Outline each blood parasite and name the species.
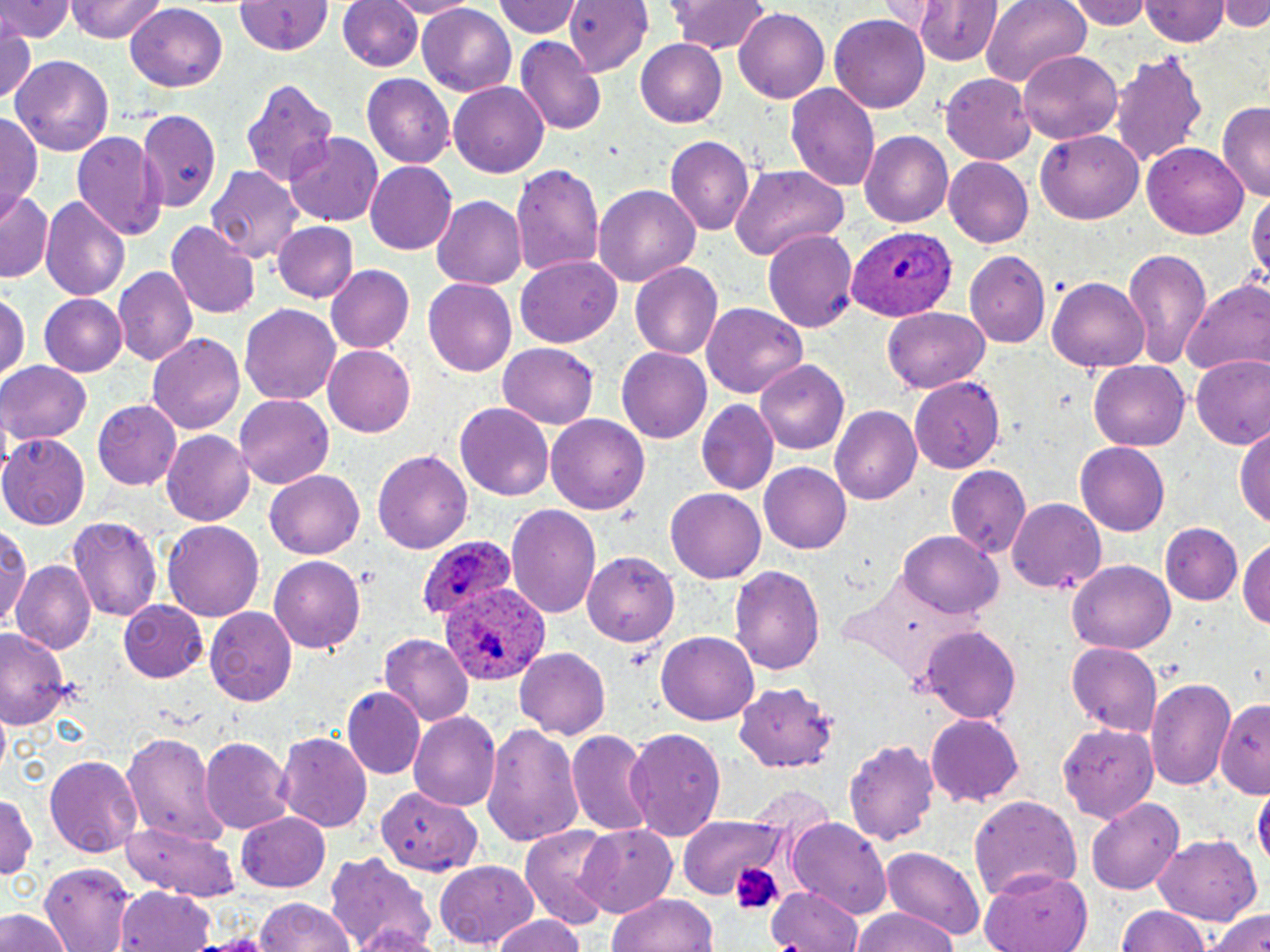
Approximate bounding boxes as [x1, y1, x2, y2] in pixels.
Plasmodium ovale-infected red blood cells: [848, 227, 956, 321], [420, 536, 516, 619], [444, 582, 551, 684].
No Plasmodium falciparum, Plasmodium malariae, Plasmodium vivax, Babesia divergens, or Trypanosoma brucei observed.

Uninfected red blood cell locations: [0, 0, 73, 42], [67, 0, 167, 42], [233, 0, 335, 55], [389, 0, 478, 17], [492, 0, 584, 39], [564, 0, 654, 75], [668, 0, 772, 54], [877, 0, 944, 37], [1071, 0, 1154, 31], [1219, 0, 1270, 29], [338, 1, 420, 73], [982, 1, 1090, 88], [1141, 1, 1230, 47], [911, 2, 1006, 66], [418, 5, 517, 95], [125, 6, 229, 91], [735, 7, 829, 103], [830, 14, 931, 112], [0, 20, 38, 104], [517, 34, 608, 137], [635, 38, 728, 129], [1112, 50, 1209, 168], [1018, 51, 1123, 145], [12, 55, 115, 156], [942, 72, 1037, 163], [361, 75, 455, 166], [240, 78, 338, 187], [449, 83, 549, 177], [787, 83, 880, 196], [1217, 102, 1270, 203], [138, 110, 221, 212], [0, 114, 42, 213], [72, 129, 166, 241], [1036, 129, 1144, 223], [286, 131, 387, 225], [861, 132, 952, 228], [665, 136, 753, 237], [1142, 145, 1250, 238], [945, 157, 1033, 248], [511, 162, 606, 276], [205, 163, 307, 265], [365, 163, 457, 253], [729, 164, 848, 262], [592, 185, 700, 288], [1246, 185, 1269, 290], [2, 191, 56, 284], [41, 196, 130, 303], [432, 196, 528, 289], [167, 221, 260, 317], [271, 223, 357, 302], [763, 228, 859, 332], [1121, 249, 1211, 366], [966, 251, 1051, 345], [516, 259, 621, 346], [629, 263, 721, 359], [326, 265, 414, 353], [112, 267, 195, 366], [1048, 277, 1148, 372], [422, 279, 516, 377], [1183, 282, 1269, 378], [0, 290, 27, 383], [39, 295, 127, 377], [239, 302, 341, 405], [702, 302, 807, 398], [885, 307, 993, 393], [147, 331, 245, 433], [498, 342, 599, 428], [323, 344, 416, 437], [617, 349, 712, 442], [1190, 358, 1269, 451], [756, 360, 850, 452], [1088, 360, 1191, 451], [0, 362, 91, 444], [907, 377, 1007, 471], [233, 393, 335, 491], [92, 398, 182, 490], [697, 399, 777, 495], [455, 402, 555, 502], [832, 405, 922, 507], [545, 415, 649, 516], [1235, 426, 1270, 528], [162, 431, 255, 525], [0, 434, 88, 527], [1075, 442, 1168, 537], [373, 445, 473, 554], [759, 462, 852, 555], [947, 466, 1032, 559], [265, 469, 366, 559], [666, 489, 766, 583], [1007, 497, 1107, 592], [507, 504, 601, 620], [67, 516, 161, 620], [1, 520, 31, 632], [164, 520, 263, 618], [1161, 522, 1241, 604], [899, 529, 1001, 618], [1242, 534, 1270, 630], [584, 552, 679, 646], [267, 553, 370, 656], [1069, 559, 1177, 654], [12, 561, 96, 656], [730, 564, 825, 676], [119, 599, 209, 682], [205, 605, 296, 704], [920, 627, 1022, 722], [0, 628, 74, 729], [655, 632, 757, 728], [377, 633, 472, 725], [1065, 640, 1164, 738], [515, 648, 611, 738], [1147, 676, 1233, 789], [735, 681, 839, 774], [344, 688, 426, 779], [1217, 702, 1269, 798], [409, 711, 499, 811], [926, 711, 1025, 804], [480, 721, 585, 848], [1056, 722, 1161, 823], [566, 729, 657, 837], [624, 729, 727, 840], [274, 730, 373, 833], [121, 733, 220, 842], [844, 736, 940, 845], [201, 739, 293, 836], [43, 754, 143, 859], [380, 780, 487, 879], [747, 785, 835, 837], [1253, 786, 1269, 874], [0, 789, 37, 887], [968, 793, 1080, 904], [1086, 797, 1183, 895], [235, 811, 328, 893], [678, 818, 789, 902], [787, 820, 892, 916], [121, 822, 241, 900], [575, 824, 677, 917], [518, 827, 615, 930], [1150, 834, 1262, 925], [878, 845, 987, 942], [324, 848, 437, 951], [434, 860, 538, 948], [43, 864, 137, 949], [980, 871, 1093, 952], [760, 882, 870, 952], [764, 885, 867, 952], [118, 887, 218, 952], [606, 892, 720, 952], [253, 897, 356, 952], [1112, 907, 1217, 952], [1206, 907, 1270, 952], [0, 909, 71, 952], [850, 909, 959, 952], [490, 911, 590, 952], [190, 933, 281, 952]. Platelet locations: [728, 856, 784, 916]. Slide-level diagnosis: Plasmodium ovale. Light microscopy. May-Grünwald-Giemsa-stained preparation. Image is 1270×952 pixels. Thin blood smear. 1000x magnification. One field of a larger specimen.